Identify the cell.
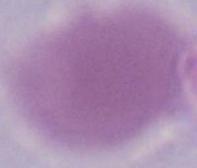

This is an erythrocyte.

Summary:
  - Modality: micrograph
  - Magnification: 1000x